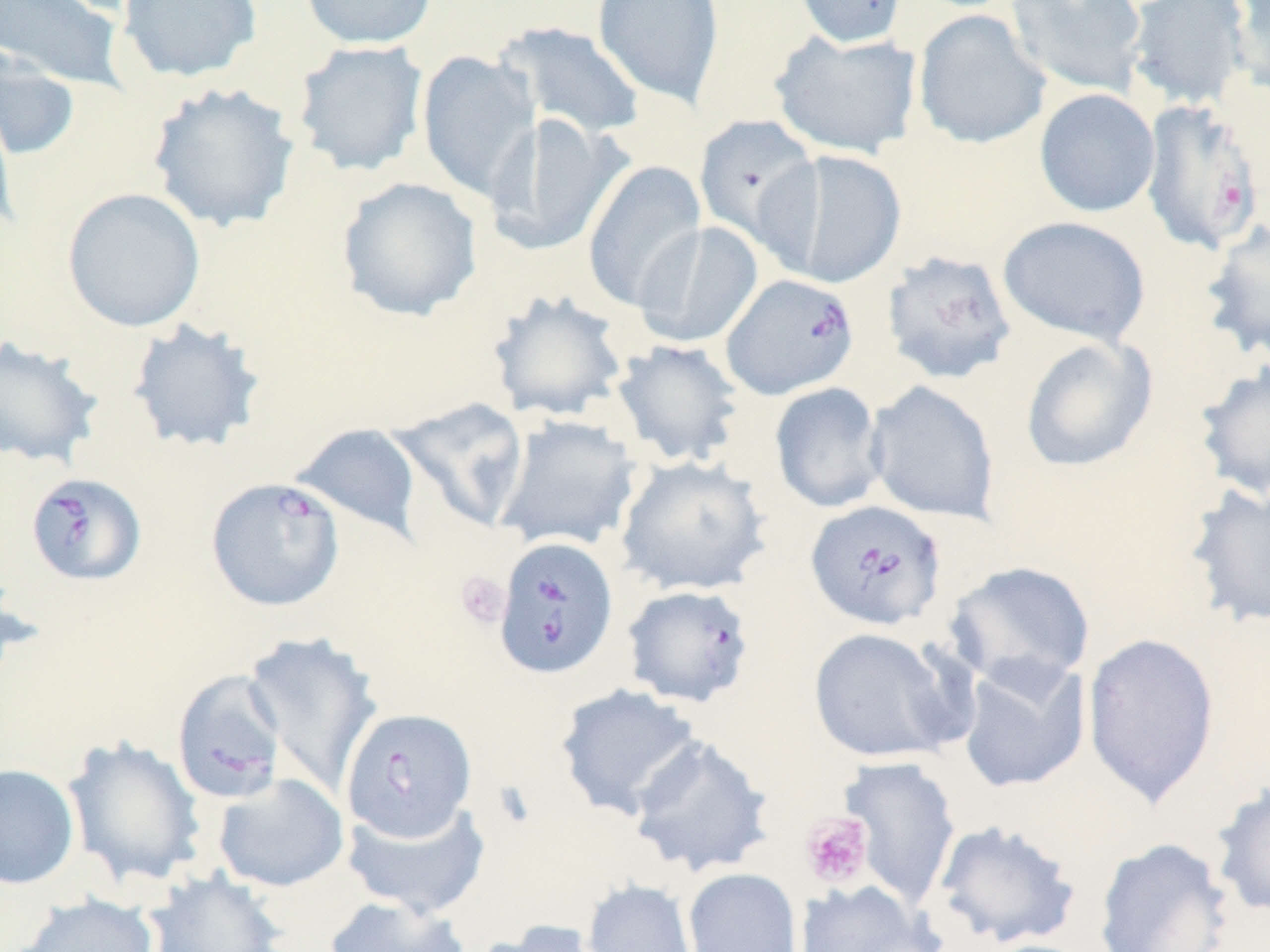

slide-level diagnosis = Babesia divergens
modality = light microscopy
preparation = thin blood smear
uninfected red blood cell locations = approximate bounding boxes as [x1, y1, x2, y2] in pixels: [0, 0, 129, 92], [116, 0, 263, 83], [299, 0, 439, 50], [592, 0, 725, 109], [790, 0, 909, 48], [1005, 0, 1148, 98], [1124, 0, 1253, 110], [1227, 1, 1270, 99], [913, 9, 1050, 150], [495, 20, 647, 141], [769, 28, 924, 159], [291, 40, 429, 177], [0, 42, 80, 161], [416, 50, 541, 201], [147, 81, 301, 233], [1034, 88, 1160, 218], [0, 93, 19, 238], [485, 113, 628, 256], [693, 114, 822, 250], [761, 148, 908, 289], [582, 161, 707, 312], [336, 176, 483, 322], [62, 187, 206, 332], [997, 215, 1152, 347], [1199, 219, 1270, 363], [633, 221, 764, 348], [881, 250, 1017, 385], [486, 289, 630, 423], [126, 317, 268, 454], [0, 335, 105, 470], [1019, 335, 1158, 473], [609, 338, 746, 468], [1193, 358, 1270, 502], [864, 380, 1001, 525], [768, 382, 889, 514], [387, 396, 530, 534], [493, 415, 643, 553], [290, 422, 425, 540], [615, 455, 771, 596], [1183, 481, 1269, 630], [945, 560, 1095, 692], [808, 626, 962, 764], [243, 631, 383, 797], [1081, 631, 1221, 809], [956, 655, 1091, 794], [554, 684, 703, 820], [626, 733, 775, 878], [62, 736, 208, 890], [839, 755, 962, 908], [0, 763, 81, 890], [212, 773, 349, 893], [1209, 778, 1270, 918], [341, 797, 492, 919], [929, 818, 1083, 950], [1093, 836, 1235, 951], [682, 867, 803, 952], [144, 869, 287, 952], [581, 879, 699, 952], [792, 879, 942, 952], [16, 893, 160, 952], [323, 894, 471, 952], [475, 919, 617, 952]
stain = May-Grünwald-Giemsa
magnification = 1000x
image size = 1270×952 pixels
platelet locations = approximate bounding boxes as [x1, y1, x2, y2] in pixels: [455, 571, 510, 629], [799, 812, 874, 889]
Babesia divergens-infected red blood cell locations = approximate bounding boxes as [x1, y1, x2, y2] in pixels: [1138, 100, 1265, 255], [720, 272, 859, 400], [25, 472, 147, 586], [205, 476, 345, 612], [804, 499, 946, 632], [493, 535, 619, 680], [621, 584, 756, 708], [170, 668, 288, 805], [340, 707, 477, 843]
field of view = one of a larger specimen